Name the parasite shown.
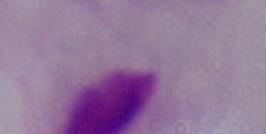
This is a trichomonad.

magnification = 1000x
modality = photomicrograph